Give the position of every Plasmodium parasite.
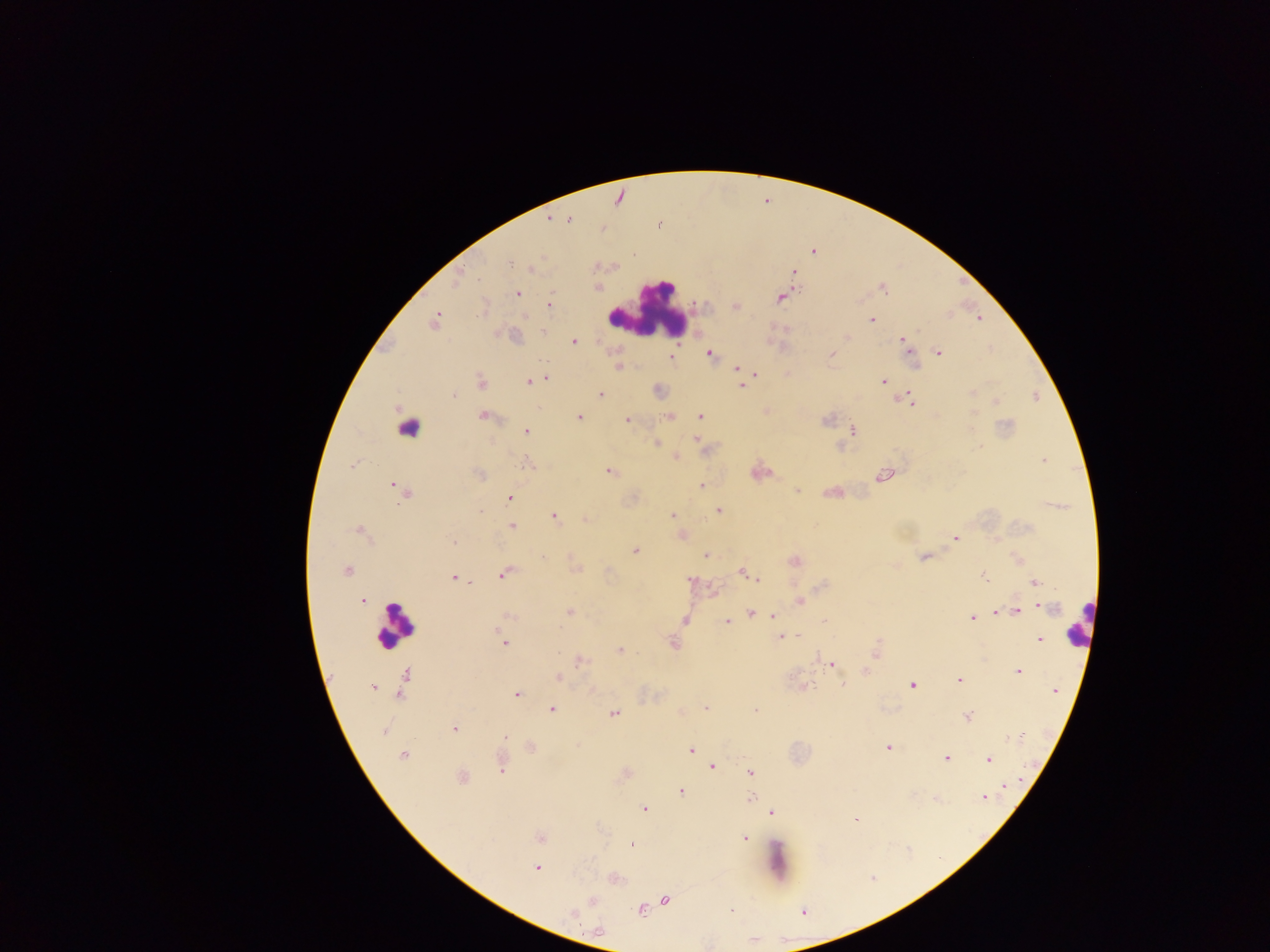

Approximate centers as (x, y) in pixels.
Plasmodium parasites: (567, 221), (660, 224), (633, 254), (510, 263), (794, 273), (459, 278), (883, 288), (517, 293), (781, 298), (550, 304), (736, 306), (979, 319), (871, 320), (434, 321), (543, 332), (845, 337), (574, 341), (903, 341), (938, 353), (709, 354), (831, 354), (670, 356), (619, 366), (737, 368), (755, 374), (546, 378), (883, 381), (481, 382), (529, 382), (741, 386), (972, 392), (601, 394), (454, 396), (909, 400), (996, 401), (483, 416), (700, 416), (579, 417), (669, 417), (627, 420), (827, 420), (853, 430), (525, 431), (696, 439), (656, 443), (979, 446), (676, 457), (1043, 461), (352, 465), (527, 465), (609, 471), (482, 475), (884, 475), (396, 486), (701, 486), (404, 490), (797, 490), (510, 498), (718, 510), (673, 515), (555, 517), (585, 520), (512, 526), (360, 532), (954, 538), (453, 542), (635, 550), (706, 556), (923, 557), (794, 561), (346, 571), (743, 571), (504, 574), (984, 576), (454, 577), (690, 579), (757, 579), (1036, 582), (799, 601), (363, 602), (1045, 607), (1017, 611), (570, 612), (750, 613), (996, 613), (509, 616), (774, 616), (971, 618), (685, 620), (825, 620), (727, 621), (797, 636), (781, 637), (1038, 640), (504, 643), (673, 643), (876, 648), (620, 651), (580, 661), (831, 664), (1019, 671), (406, 676), (558, 678), (959, 679), (843, 684), (911, 685), (372, 687), (1055, 691), (517, 695), (706, 708), (552, 709), (756, 710), (614, 714), (966, 716), (455, 729), (383, 730), (506, 736), (1018, 738), (888, 747), (691, 750), (403, 755), (696, 755), (946, 758), (989, 759), (712, 767), (501, 770), (751, 772), (462, 777), (1007, 787), (681, 792), (751, 799), (984, 799), (644, 809), (772, 812), (856, 819), (540, 838), (744, 838), (631, 845), (537, 868), (665, 899), (592, 900), (640, 910), (731, 910), (572, 913).

Leukocyte locations: (648, 313), (408, 427), (1078, 622), (394, 626). Single field of view. Collected in Ghana. Image is 1270×952 pixels. Mobile-phone photograph taken through the microscope. Thick blood film.